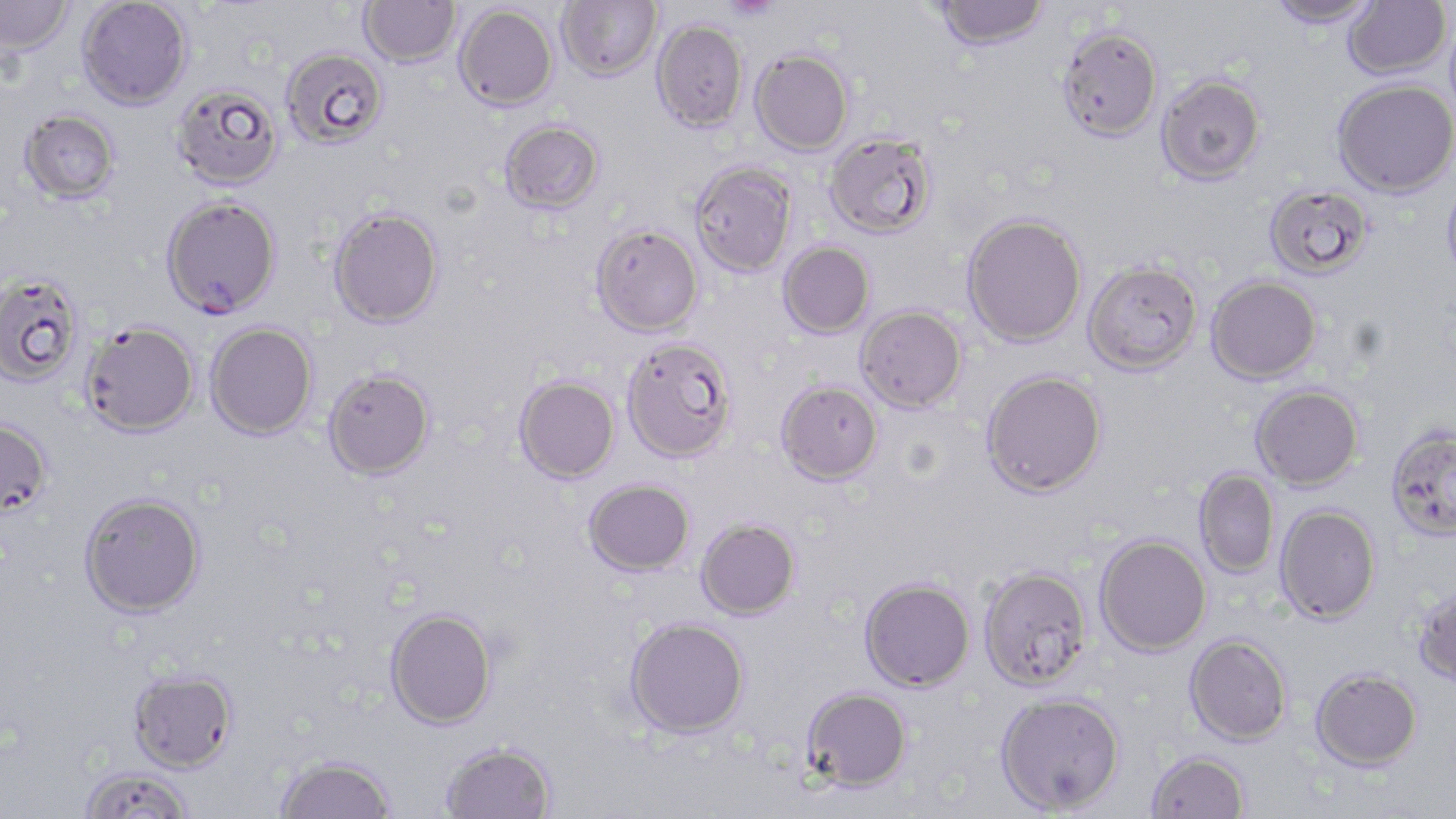
slide-level diagnosis = Plasmodium falciparum
preparation = thin blood smear
field of view = one of a larger specimen
image size = 1456×819 pixels
uninfected red blood cell locations = approximate bounding boxes as (x1, y1, x2, y2) in pixels: (0, 0, 74, 58), (77, 0, 191, 111), (359, 0, 461, 68), (556, 0, 661, 81), (1265, 0, 1382, 27), (933, 1, 1050, 51), (1343, 1, 1451, 80), (454, 4, 558, 111), (652, 20, 748, 132), (1056, 26, 1163, 142), (280, 47, 389, 149), (750, 49, 853, 155), (1157, 74, 1265, 185), (1332, 79, 1456, 197), (171, 83, 284, 191), (19, 109, 121, 204), (499, 119, 605, 215), (824, 131, 938, 240), (690, 162, 796, 276), (1441, 173, 1456, 288), (1264, 184, 1374, 280), (328, 207, 445, 330), (961, 212, 1087, 348), (591, 223, 703, 336), (778, 242, 875, 338), (1083, 260, 1203, 375), (0, 273, 84, 387), (1206, 275, 1322, 384), (856, 305, 967, 413), (81, 322, 199, 440), (204, 323, 317, 442), (621, 336, 738, 462), (322, 369, 435, 481), (981, 370, 1107, 497), (514, 375, 620, 483), (776, 380, 883, 485), (1251, 385, 1364, 491), (0, 418, 54, 522), (1385, 425, 1456, 541), (1193, 468, 1280, 580), (583, 478, 695, 576), (78, 493, 207, 620), (1274, 503, 1381, 624), (696, 518, 800, 620), (1095, 535, 1211, 656), (979, 566, 1092, 690), (859, 576, 975, 692), (1412, 583, 1456, 687), (384, 608, 498, 730), (624, 616, 750, 738), (1184, 633, 1292, 746), (1311, 667, 1422, 770), (128, 671, 238, 776), (800, 686, 912, 791), (994, 691, 1125, 815), (439, 741, 556, 819), (1146, 750, 1250, 818), (274, 756, 396, 819), (79, 769, 194, 819)
magnification = 1000x
modality = optical microscopy
Plasmodium falciparum-infected red blood cell locations = approximate bounding boxes as (x1, y1, x2, y2) in pixels: (160, 196, 283, 321)
stain = May-Grünwald-Giemsa